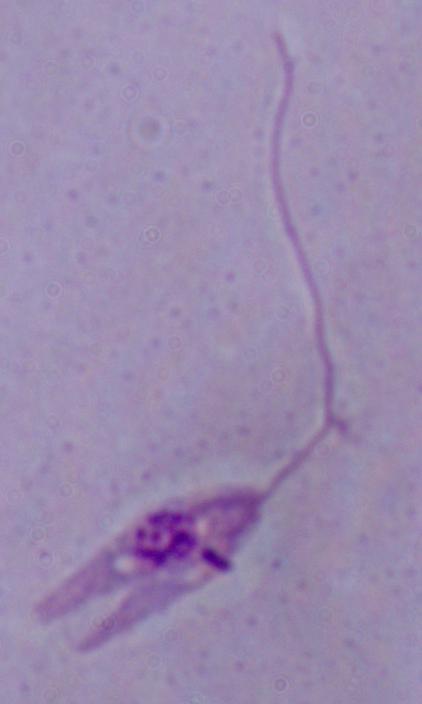

Captured at 1000x magnification. A Leishmania parasite is seen. Micrograph.